Name the parasite shown.
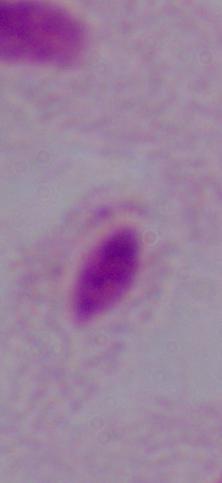

This is a trichomonad.

Summary:
  - Magnification: 1000x
  - Modality: photomicrograph